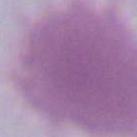

identification: red blood cell
magnification: 1000x
modality: photomicrograph